Classify this cell by malaria status.
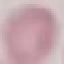
It is uninfected.

capture = smartphone through the microscope eyepiece
image type = cell patch, automatically extracted from a larger field of view and resized to 64 × 64 pixels
preparation = thin blood smear
stain = Giemsa